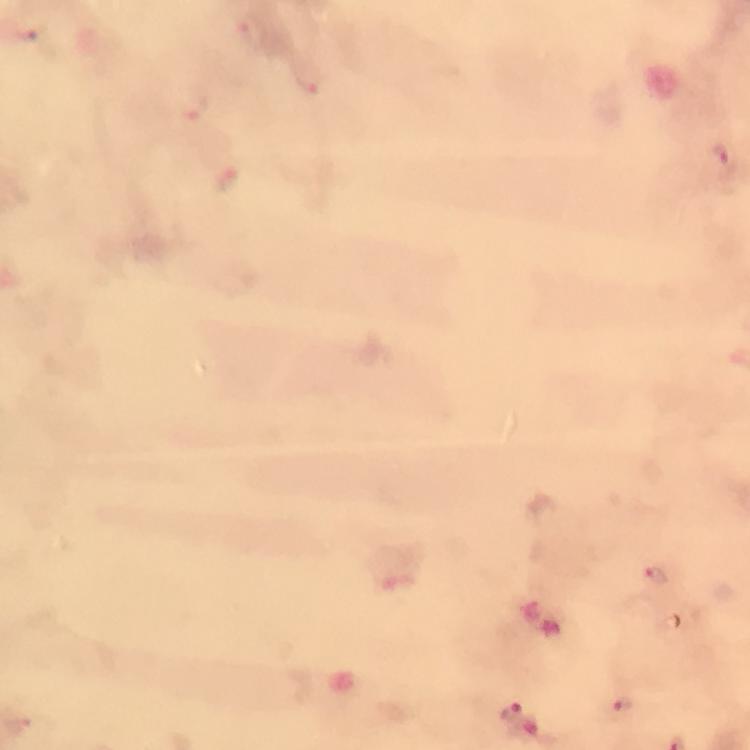
Approximate centers as [x, y] in pixels. Plasmodium parasite locations: [252, 32], [308, 79], [195, 106], [721, 156], [229, 178], [656, 578], [512, 709], [623, 709]. Immersion oil applied. Giemsa-stained preparation. Photographed with a smartphone mounted on the microscope. From a malaria diagnostic workup. 100x magnification. Cropped region of a single field of view. Thick blood film. Image is 750×750 pixels.